Classify this cell by malaria status.
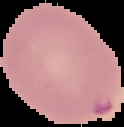

It is parasitized.

The area outside the segmented cell region is set to black. From a thin blood smear. Image is 124×127 pixels.